Describe the morphology of the erythrocytes.
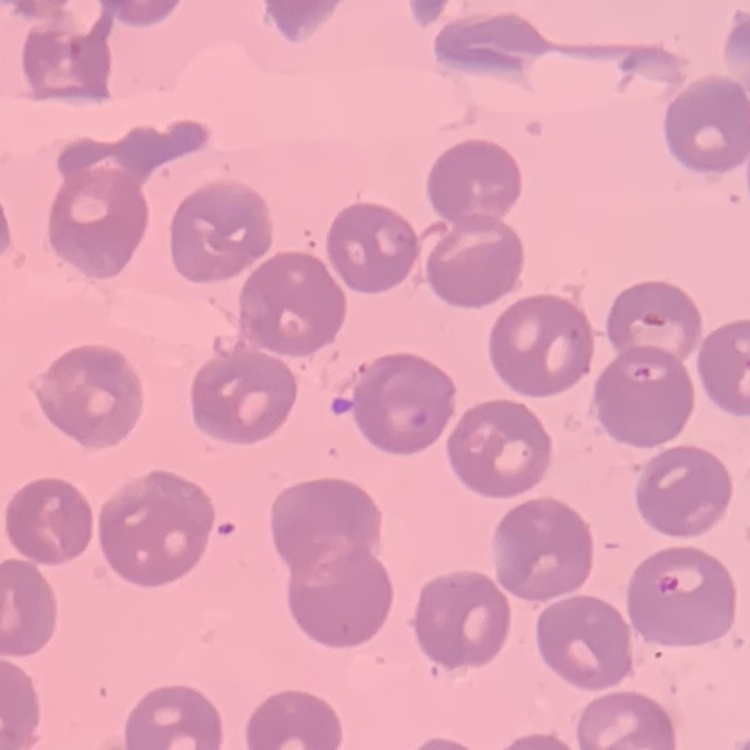

No rouleaux formation.

Summary:
  - Preparation: thin blood smear
  - Image type: square crop of a larger photomicrograph
  - Stain: Field's or Giemsa